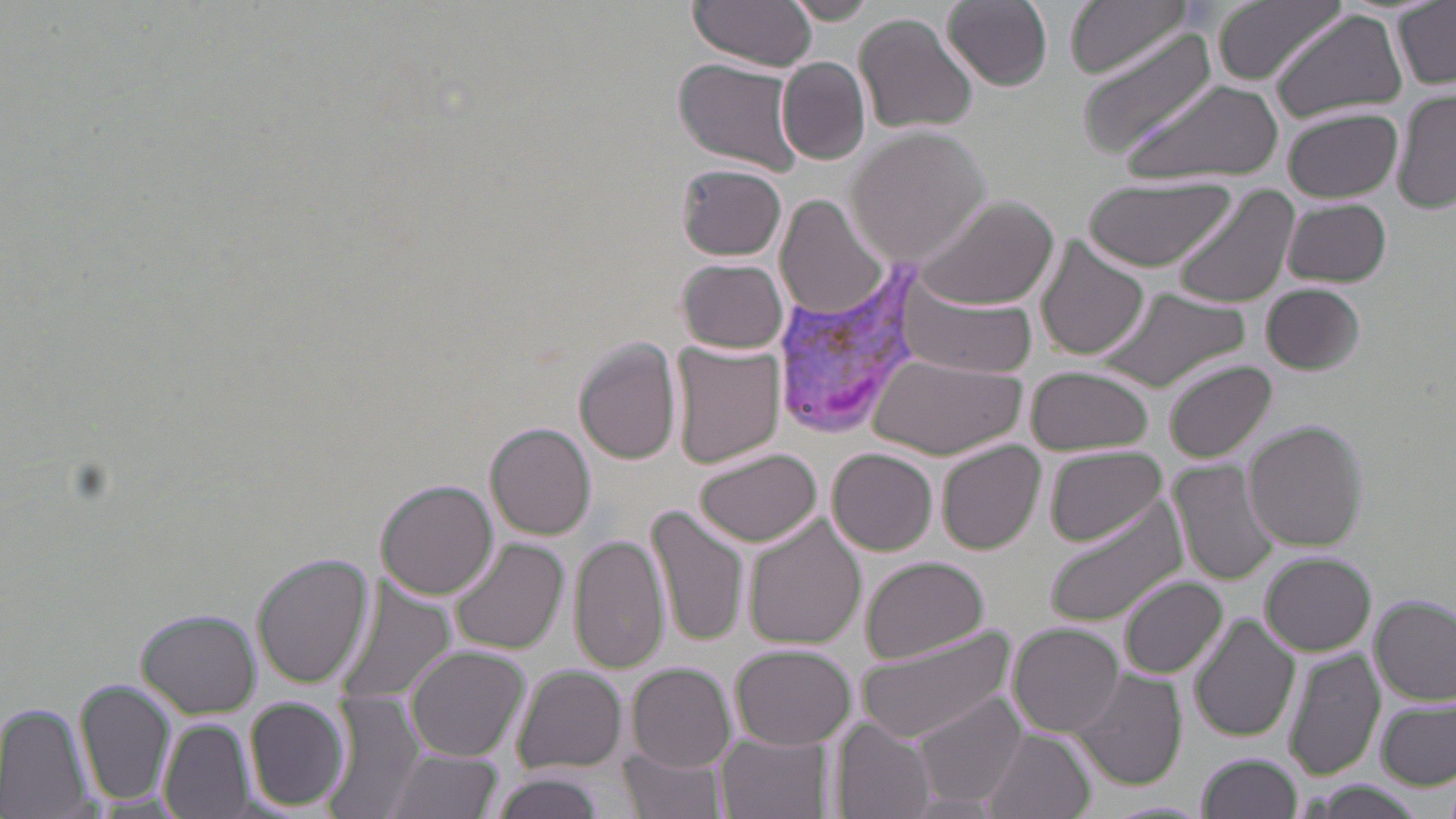

Summary:
  - Coordinate format: approximate bounding boxes as [x1, y1, x2, y2] in pixels
  - Plasmodium vivax-infected red blood cell locations: [770, 265, 929, 441]
  - Uninfected red blood cell locations: [688, 0, 817, 70], [783, 0, 877, 24], [942, 0, 1053, 90], [1067, 0, 1190, 78], [1212, 0, 1348, 85], [1393, 2, 1455, 88], [1270, 7, 1406, 121], [852, 12, 978, 136], [1078, 31, 1221, 160], [671, 58, 807, 175], [778, 58, 869, 164], [1120, 78, 1283, 185], [1393, 87, 1456, 217], [1280, 106, 1402, 201], [847, 127, 992, 264], [675, 163, 786, 261], [1077, 176, 1236, 270], [1172, 183, 1300, 309], [910, 195, 1060, 311], [776, 196, 888, 319], [1281, 198, 1392, 288], [1031, 235, 1149, 362], [677, 258, 789, 354], [896, 275, 1041, 380], [1262, 282, 1366, 374], [1094, 286, 1249, 394], [574, 338, 682, 464], [669, 339, 784, 469], [875, 353, 1026, 458], [1163, 359, 1277, 463], [1024, 365, 1155, 456], [1243, 421, 1368, 551], [487, 422, 595, 540], [937, 439, 1044, 554], [1042, 445, 1169, 546], [696, 448, 822, 545], [829, 448, 937, 555], [1172, 459, 1281, 587], [376, 480, 498, 598], [1043, 495, 1189, 627], [646, 504, 752, 647], [745, 516, 864, 648], [569, 528, 668, 675], [447, 537, 568, 655], [254, 553, 372, 689], [1261, 553, 1375, 655], [860, 555, 990, 663], [1119, 576, 1228, 679], [329, 582, 454, 714], [1371, 596, 1455, 706], [137, 610, 260, 717], [1189, 612, 1300, 742], [1010, 623, 1124, 736], [854, 625, 1014, 744], [405, 643, 529, 761], [731, 643, 852, 749], [1282, 646, 1383, 784], [629, 662, 735, 772], [515, 664, 627, 773], [1069, 669, 1185, 790], [76, 675, 175, 810], [914, 690, 1029, 809], [323, 691, 427, 819], [244, 696, 350, 811], [1377, 697, 1456, 788], [0, 702, 92, 818], [160, 718, 252, 819], [832, 718, 941, 819], [983, 728, 1094, 819], [719, 732, 826, 819], [620, 746, 726, 819], [382, 748, 501, 819], [1194, 751, 1303, 818], [488, 772, 607, 819], [905, 792, 1003, 817]
  - Slide-level diagnosis: Plasmodium vivax
  - Stain: May-Grünwald-Giemsa
  - Modality: optical microscopy
  - Magnification: 1000x
  - Image size: 1456×819 pixels
  - Field of view: single
  - Preparation: thin blood film